Outline each blood parasite and name the species.
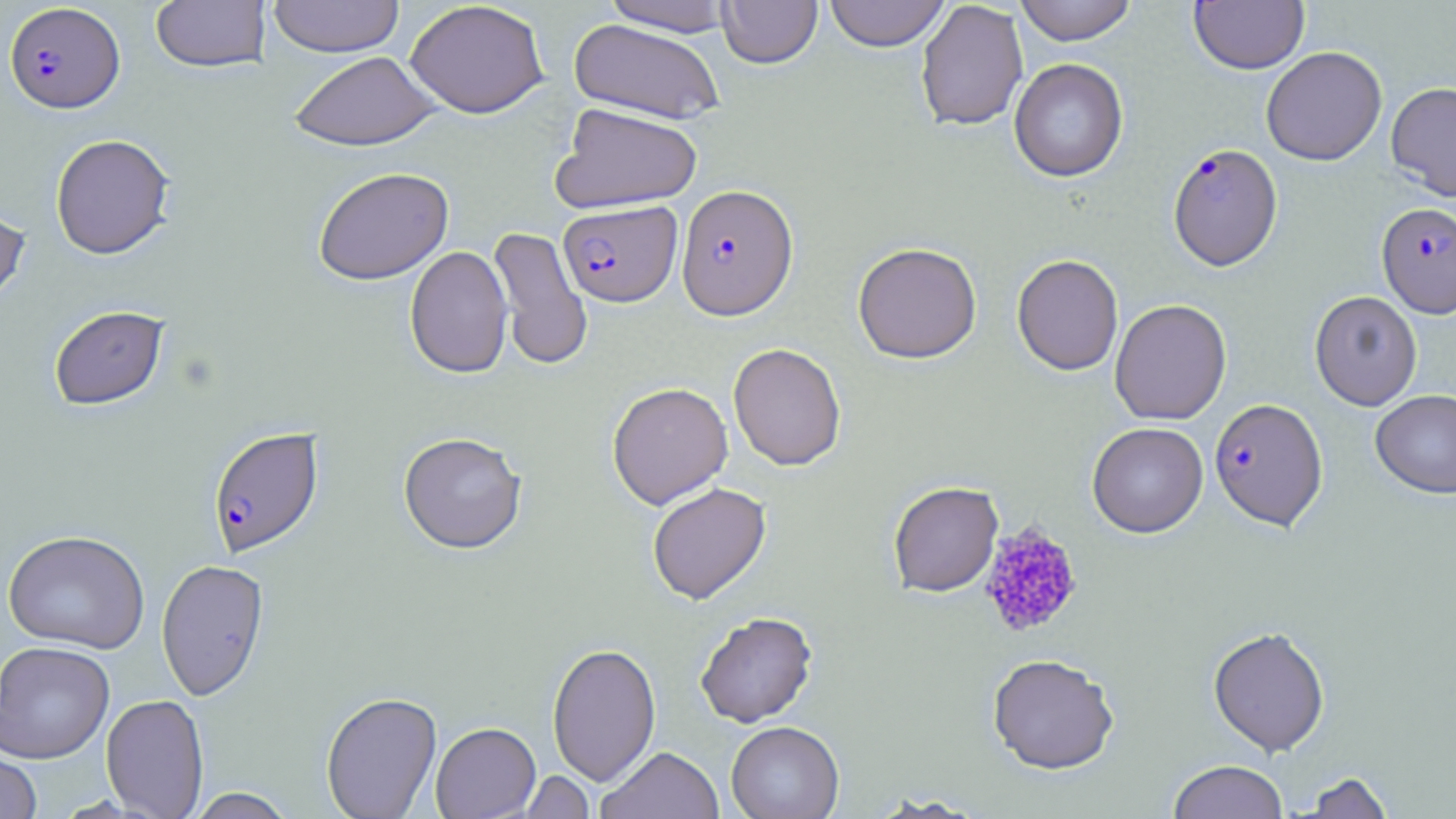

Approximate bounding boxes as (x1, y1, x2, y2) in pixels.
Plasmodium falciparum-infected red blood cells: (4, 2, 125, 113), (1168, 143, 1283, 271), (676, 183, 799, 320), (558, 201, 682, 307), (1377, 202, 1456, 318), (1209, 398, 1328, 530), (207, 425, 325, 557).
No Plasmodium ovale, Plasmodium malariae, Plasmodium vivax, Babesia divergens, or Trypanosoma brucei observed.

Uninfected red blood cell locations: (268, 0, 404, 58), (600, 0, 739, 36), (717, 0, 822, 68), (824, 0, 950, 51), (915, 0, 1028, 132), (1015, 0, 1137, 45), (1189, 0, 1309, 74), (151, 1, 270, 73), (405, 1, 550, 119), (568, 19, 726, 124), (1261, 46, 1387, 166), (289, 51, 440, 150), (1009, 58, 1128, 182), (1386, 81, 1456, 201), (551, 102, 703, 214), (50, 133, 176, 260), (312, 166, 454, 285), (0, 200, 31, 312), (487, 226, 593, 370), (852, 242, 982, 364), (405, 246, 513, 378), (1012, 254, 1123, 375), (1309, 291, 1422, 410), (1109, 298, 1232, 425), (48, 304, 169, 410), (728, 342, 846, 471), (606, 381, 733, 509), (1371, 390, 1456, 498), (1087, 422, 1208, 538), (398, 431, 528, 554), (888, 481, 1003, 597), (647, 482, 771, 604), (3, 529, 150, 653), (156, 558, 269, 700), (695, 611, 818, 727), (1207, 626, 1330, 756), (0, 641, 115, 763), (547, 642, 661, 785), (987, 653, 1120, 775), (320, 691, 442, 818), (100, 694, 210, 818), (726, 721, 844, 819), (430, 722, 541, 818), (598, 745, 724, 819), (0, 748, 42, 819), (1168, 760, 1288, 819), (519, 770, 595, 818), (1299, 771, 1396, 818), (186, 788, 297, 818). Platelet locations: (979, 522, 1082, 639). Slide-level diagnosis: Plasmodium falciparum. Image is 1456×819 pixels. One field of a larger specimen. 1000x magnification. Thin blood smear. May-Grünwald-Giemsa-stained preparation. Optical microscopy.